Report the malaria status of this cell.
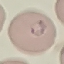
Parasitized.

Summary:
  - Stain: Giemsa
  - Preparation: thin smear
  - Image type: cell patch, automatically extracted from a larger field of view and resized to 64 × 64 pixels
  - Capture: smartphone camera at the microscope eyepiece